Classify this cell by malaria status.
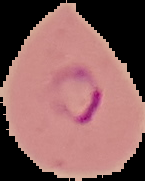

It is parasitized.

Cell region segmented out of the field of view; the surrounding area is masked to black. From a thin blood film. Image is 145×181 pixels.